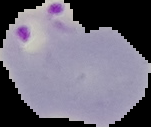
Image is 151×127 pixels. Malaria status: parasitized. The area outside the segmented cell region is set to black. From a thin blood film.